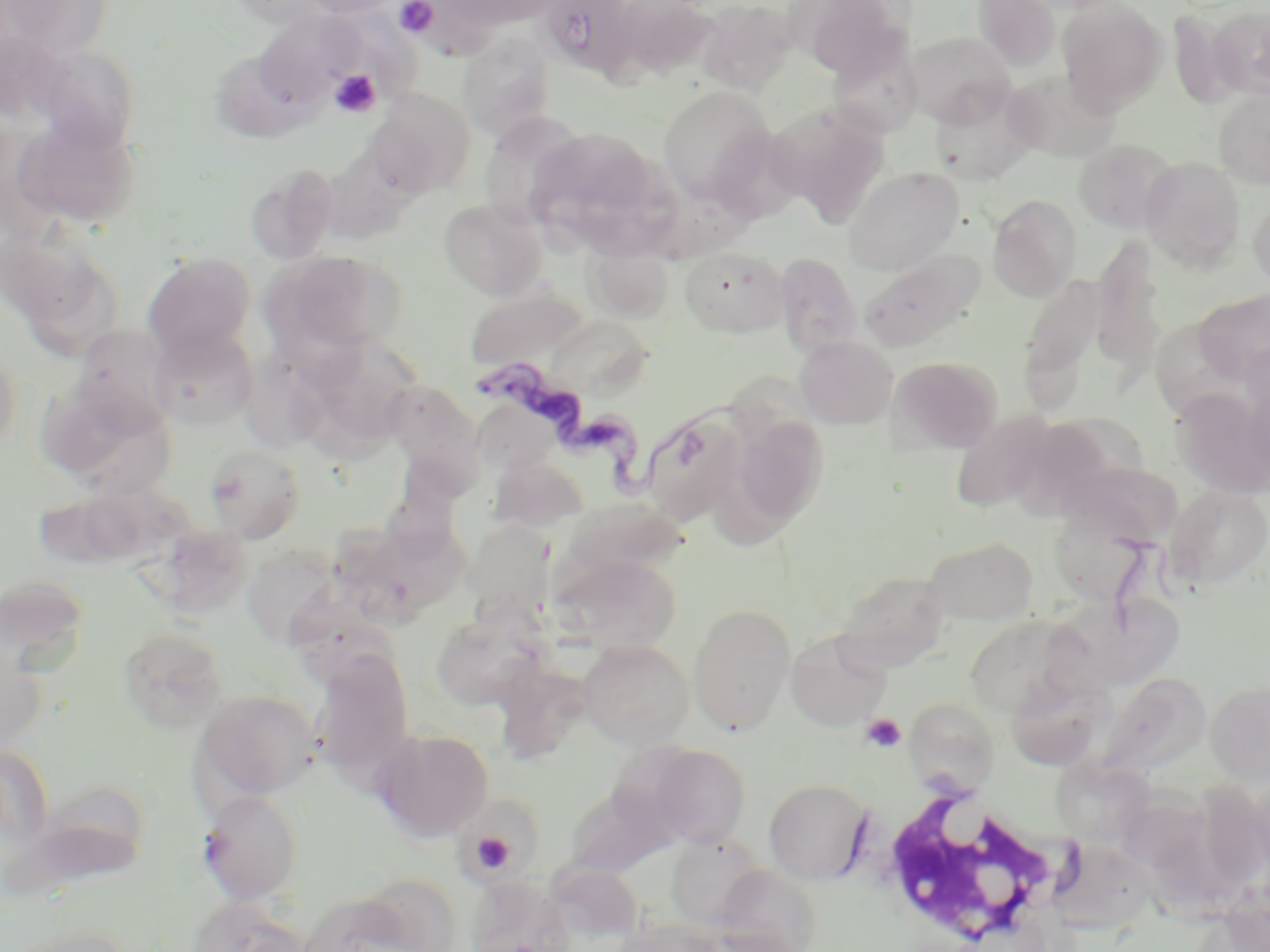

Approximate bounding boxes as (x1,y1)-(x2,y2) corner pairs in pixels. Platelet locations: (394,0)-(438,37), (328,70)-(381,118), (860,713)-(906,753), (467,827)-(523,877). Uninfected red blood cell locations: (1,0)-(116,59), (223,0)-(338,29), (299,0)-(405,17), (449,0)-(562,28), (540,0)-(638,88), (608,0)-(720,86), (785,0)-(909,77), (972,0)-(1062,71), (1057,0)-(1167,114), (696,1)-(799,93), (1209,5)-(1270,101), (1168,8)-(1241,110), (252,9)-(365,110), (904,30)-(1015,128), (459,34)-(556,139), (827,35)-(924,138), (36,45)-(141,151), (222,55)-(326,143), (1005,67)-(1121,162), (929,81)-(1039,186), (657,85)-(774,203), (366,88)-(476,198), (1213,89)-(1270,189), (768,103)-(890,228), (479,112)-(588,229), (17,115)-(143,230), (706,124)-(803,227), (528,127)-(663,252), (1073,138)-(1178,233), (1139,157)-(1246,271), (245,165)-(339,266), (844,167)-(963,276), (988,194)-(1082,301), (1248,195)-(1270,292), (439,198)-(548,300), (6,232)-(123,359), (1091,237)-(1167,382), (586,242)-(674,323), (679,245)-(791,338), (268,249)-(407,359), (858,249)-(983,352), (143,252)-(256,357), (775,252)-(863,357), (1018,273)-(1104,407), (464,287)-(589,373), (1195,290)-(1270,386), (545,313)-(655,400), (71,324)-(177,430), (148,327)-(258,430), (794,335)-(898,430), (317,336)-(421,439), (237,339)-(346,455), (1242,340)-(1270,419), (0,345)-(22,455), (887,355)-(1003,455), (384,379)-(484,489), (37,382)-(174,498), (1169,386)-(1270,498), (639,407)-(747,527), (951,410)-(1058,513), (724,411)-(830,535), (1021,415)-(1145,517), (205,445)-(306,543), (489,455)-(590,534), (1057,462)-(1191,540), (1164,485)-(1270,589), (32,489)-(152,571), (558,496)-(688,585), (1054,503)-(1162,611), (469,520)-(560,619), (357,528)-(478,639), (924,535)-(1038,626), (241,542)-(347,648), (553,551)-(681,654), (832,570)-(951,672), (0,576)-(91,678), (1067,599)-(1186,696), (688,603)-(796,734), (430,610)-(546,710), (964,613)-(1088,717), (119,626)-(229,733), (785,631)-(891,730), (0,639)-(46,755), (578,640)-(694,748), (310,649)-(415,783), (498,668)-(593,769), (1099,672)-(1211,777), (1206,681)-(1270,786), (194,690)-(319,802), (907,699)-(1010,795), (373,727)-(494,841), (643,743)-(751,849), (1051,757)-(1155,847), (1105,775)-(1223,880), (764,778)-(872,885), (30,780)-(152,883), (564,782)-(672,878), (197,789)-(303,904), (456,799)-(537,881), (667,835)-(768,930), (1056,844)-(1159,935), (715,865)-(822,952), (465,875)-(576,952), (296,891)-(438,952), (1203,897)-(1268,951), (185,898)-(312,952), (614,919)-(723,952), (7,924)-(139,952). Trypanosoma brucei locations: (480,362)-(742,499). White blood cell locations: (865,788)-(1082,948). Slide-level diagnosis: Trypanosoma brucei. Captured at 1000x magnification. Image is 1270×952 pixels. One field of a larger specimen. Optical microscopy. May-Grünwald-Giemsa-stained preparation. Thin blood smear.